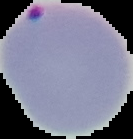

preparation = thin blood film
result = Plasmodium parasites identified
image type = segmented cell region with the area outside set to black
image size = 133×139 pixels